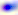
modality: micrograph
identification: Toxoplasma gondii
magnification: 400x